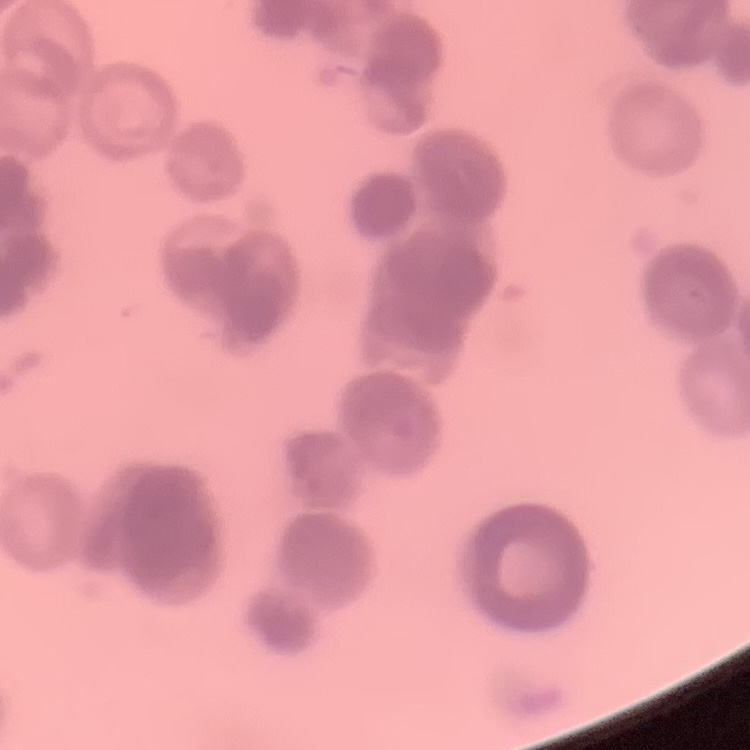 The erythrocytes show rouleaux formation. Thin blood film. Field's or Giemsa stain. One tile cut from a larger photomicrograph.